Comment on the morphology of the erythrocytes.
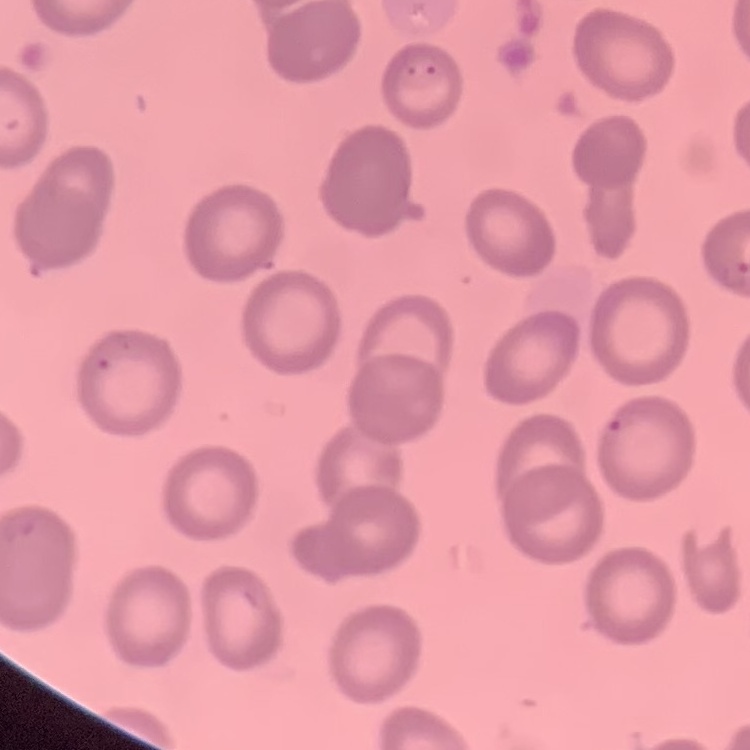

They show no rouleaux formation.

Field's or Giemsa stain. Square crop of a larger photomicrograph. Thin blood film.